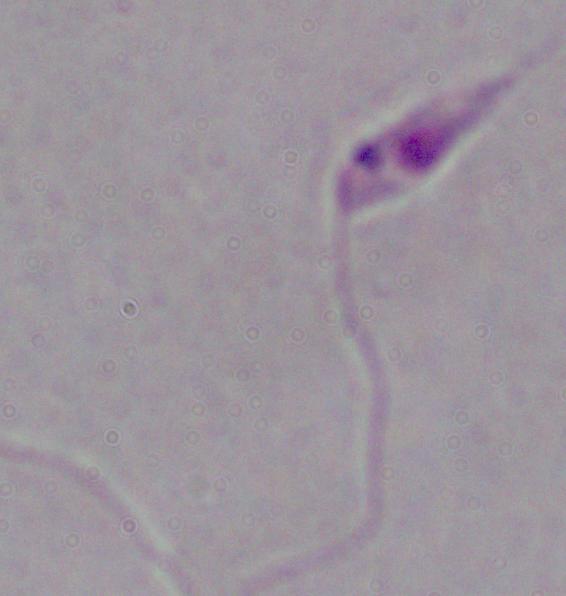
Summary:
  - Identification: Leishmania
  - Magnification: 1000x
  - Modality: photomicrograph